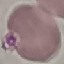
Malaria status: uninfected. Automatically extracted cell patch, resized to 64 × 64 pixels. Thin blood smear. Giemsa-stained preparation. Photographed with a smartphone camera at the microscope eyepiece.